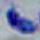
modality = photomicrograph
identification = Toxoplasma gondii
magnification = 1000x